Give the position of every Plasmodium parasite visible.
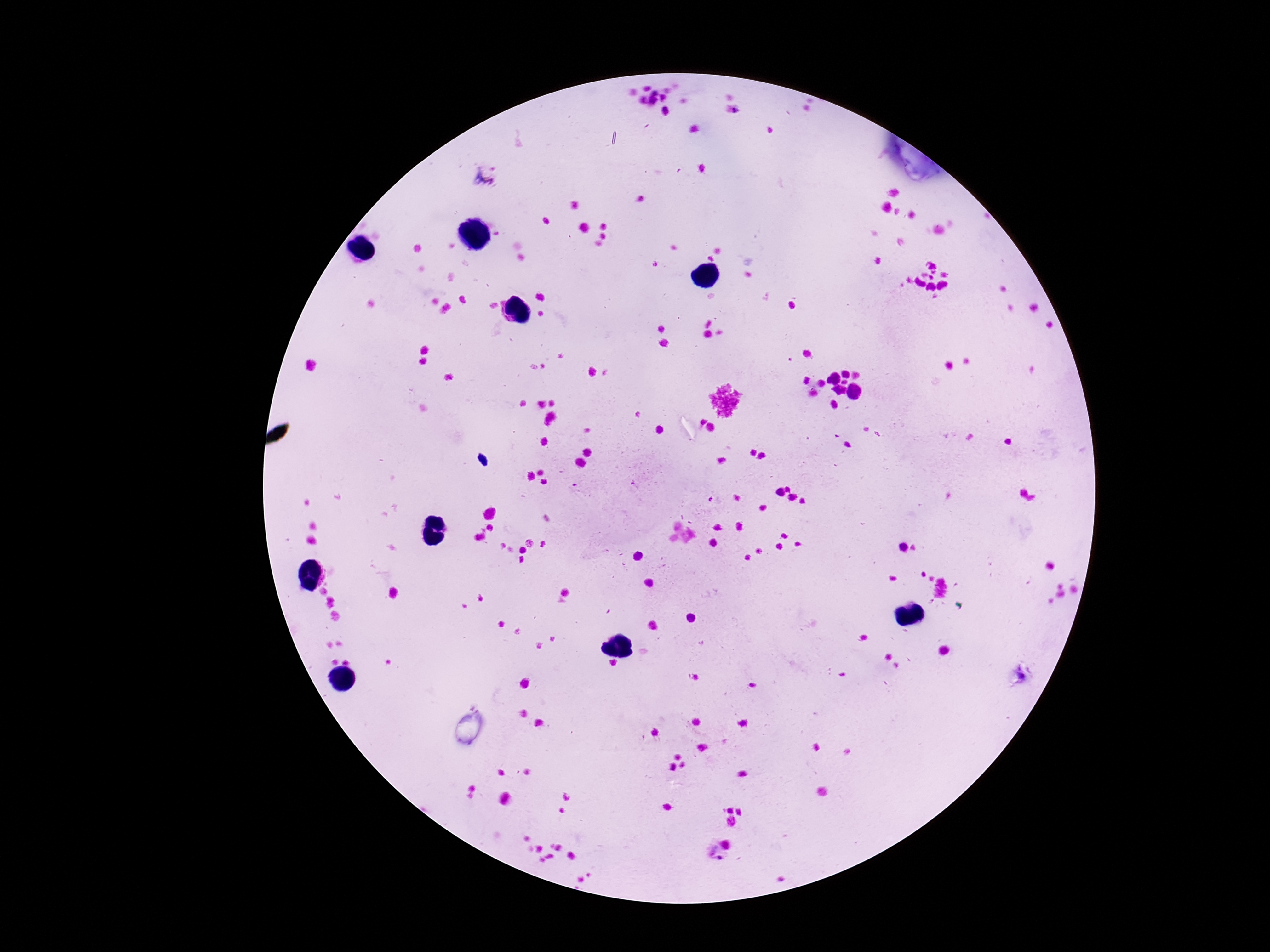

Approximate centers as (x, y) in pixels.
Plasmodium parasites: (485, 176), (636, 486), (577, 491), (715, 500).

Summary:
  - Capture: smartphone camera through the microscope eyepiece
  - Preparation: thick blood film
  - Stain: Giemsa
  - Image size: 1270×952 pixels
  - Patient malaria status: infected
  - Field of view: single
  - Magnification: 100x